Assess for malaria.
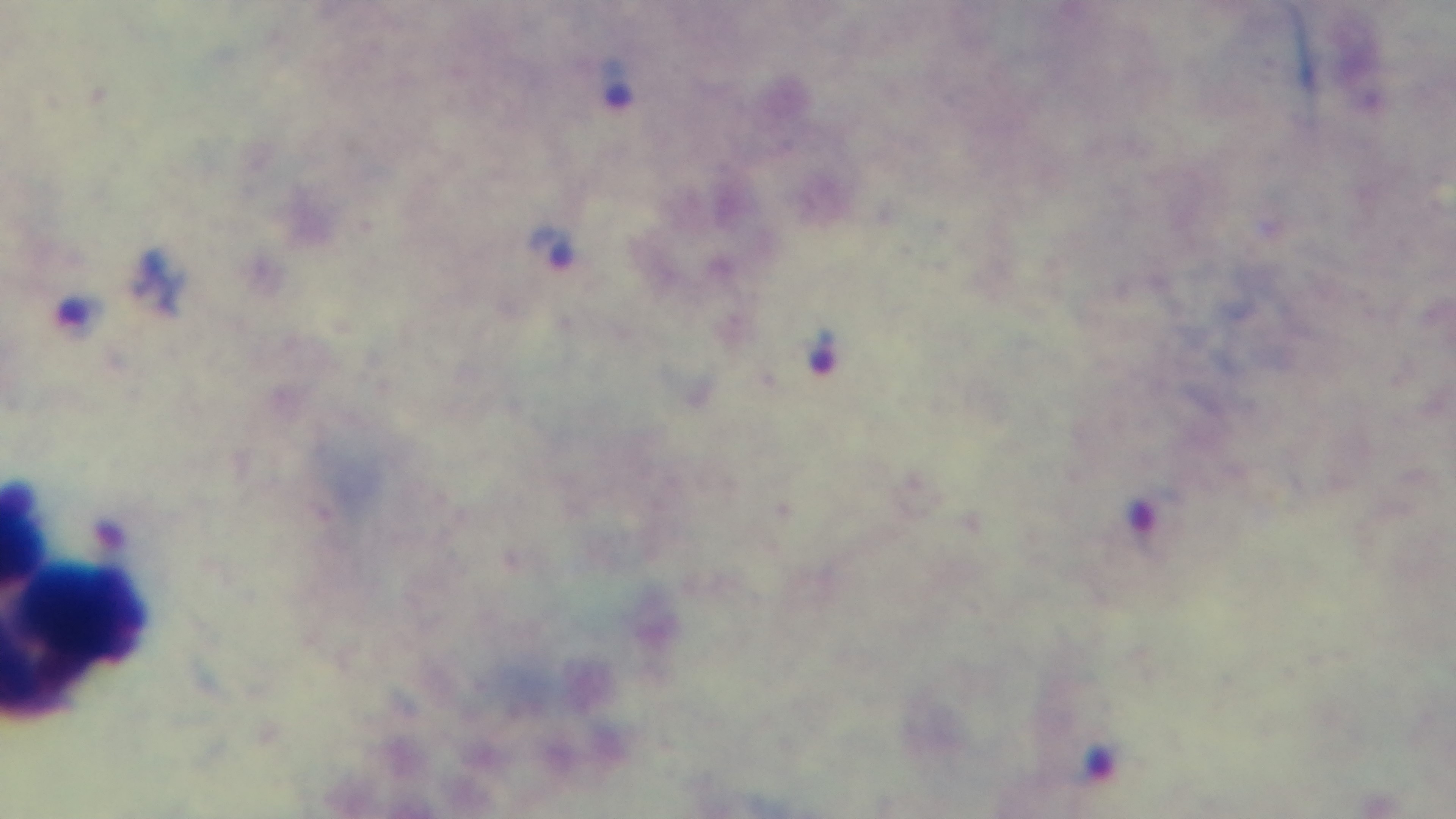
Infected.

stain = Giemsa
capture = mounted 4K digital camera
field of view = one from the slide
preparation = thick blood film
modality = light microscopy
objective = 100x oil immersion